Locate every blood parasite and identify its species.
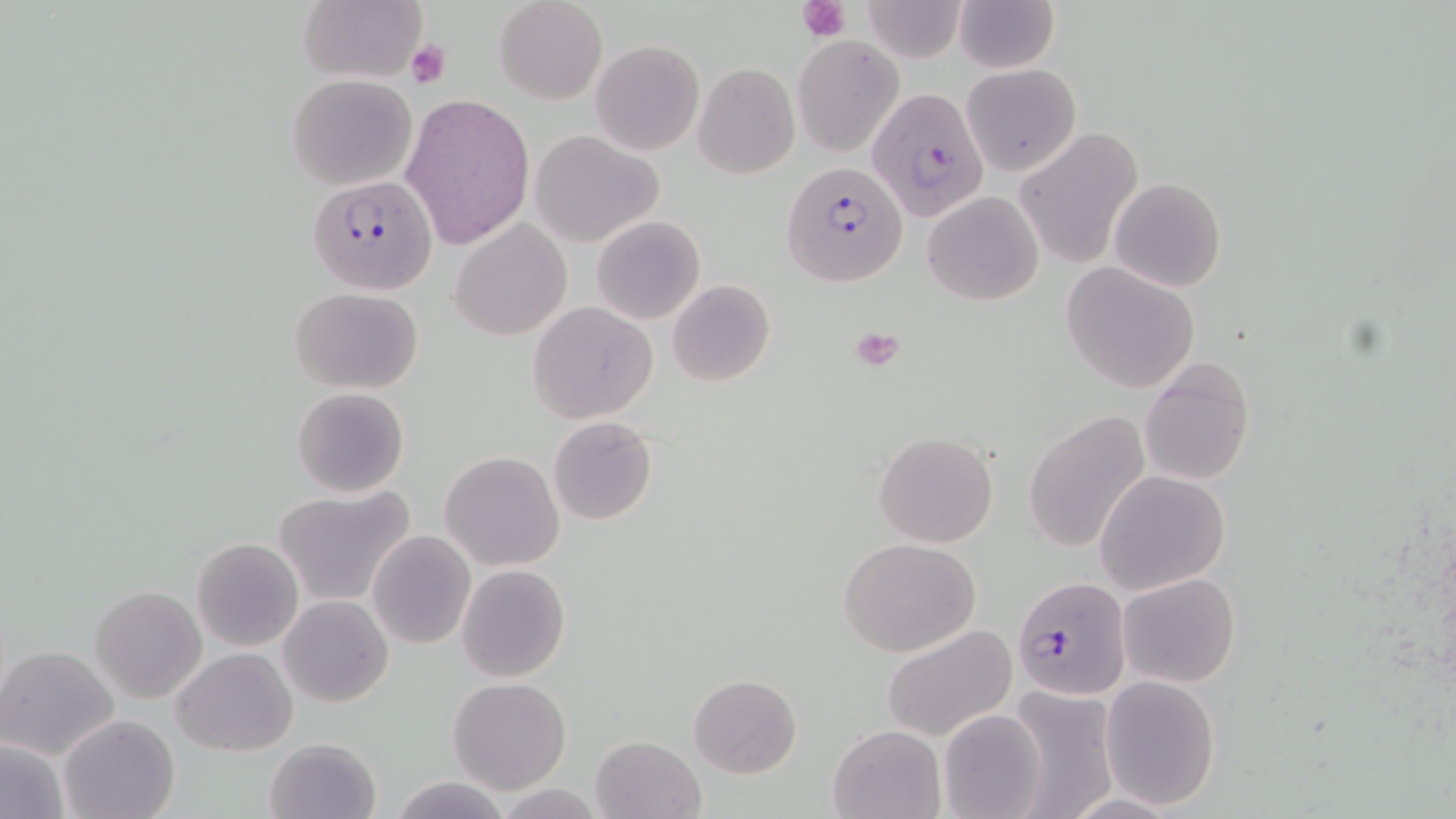

Approximate bounding boxes as (x1, y1, x2, y2) in pixels.
Plasmodium falciparum-infected red blood cells: (868, 88, 989, 220), (784, 161, 909, 285), (309, 176, 438, 296), (1012, 577, 1130, 699).
No Plasmodium ovale, Plasmodium malariae, Plasmodium vivax, Babesia divergens, or Trypanosoma brucei observed.

Platelet locations: (797, 0, 851, 43), (405, 41, 449, 88), (849, 325, 907, 371). Uninfected red blood cell locations: (297, 0, 426, 84), (495, 0, 607, 104), (860, 0, 968, 63), (954, 0, 1058, 72), (793, 34, 903, 155), (590, 39, 704, 154), (693, 62, 799, 178), (962, 63, 1081, 175), (286, 74, 416, 189), (399, 93, 535, 251), (1014, 129, 1143, 271), (530, 130, 662, 246), (1110, 177, 1226, 293), (1079, 188, 1216, 368), (923, 189, 1045, 305), (592, 216, 705, 324), (449, 218, 573, 342), (1061, 261, 1202, 393), (667, 280, 776, 387), (289, 286, 423, 393), (527, 301, 657, 423), (1140, 358, 1254, 486), (292, 387, 408, 497), (1023, 409, 1152, 554), (547, 415, 659, 525), (873, 429, 999, 548), (440, 452, 564, 571), (1095, 469, 1230, 596), (273, 487, 417, 607), (367, 531, 475, 649), (838, 536, 982, 658), (375, 537, 562, 662), (192, 538, 304, 651), (455, 563, 571, 682), (1118, 572, 1242, 688), (89, 584, 208, 704), (279, 595, 392, 707), (881, 622, 1018, 743), (1, 645, 119, 760), (173, 647, 297, 755), (688, 674, 802, 778), (1098, 677, 1221, 808), (448, 678, 573, 794), (1009, 686, 1119, 818), (938, 707, 1048, 819), (60, 714, 178, 819), (828, 723, 946, 818), (590, 735, 707, 819), (264, 737, 381, 818), (0, 739, 69, 818), (389, 775, 512, 818), (495, 782, 606, 819). Slide-level diagnosis: Plasmodium falciparum. May-Grünwald-Giemsa stain. Single field of view. Thin blood smear. 1000x magnification. Light microscopy. Image is 1456×819 pixels.